Classify this cell by malaria status.
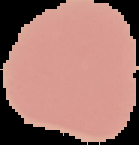

Uninfected.

{
  "image_type": "segmented cell region with the area outside set to black",
  "image_size": "139×145 pixels",
  "preparation": "thin blood film"
}